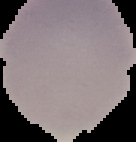
malaria status = uninfected
preparation = thin blood smear
image type = cell region segmented out of the field of view; surrounding area masked to black
image size = 136×142 pixels